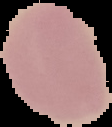 Image is 112×127 pixels. From a thin blood film. The area outside the segmented cell region is set to black. Result: negative for Plasmodium parasites.